Assess the morphology of the erythrocytes.
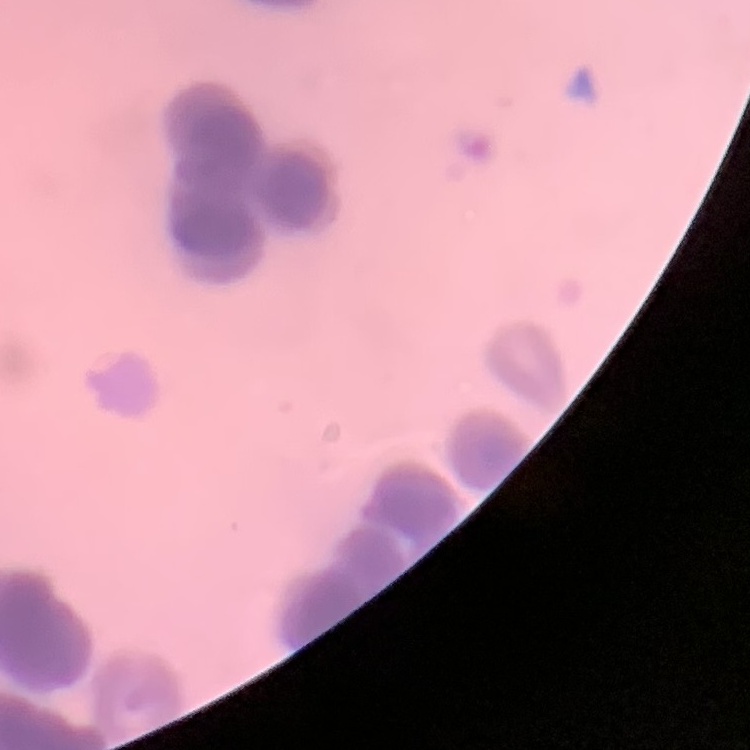

Rouleaux formation.

preparation = thin blood film
image type = square crop of a larger photomicrograph
stain = Field's or Giemsa